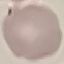 Malaria status: uninfected. Thin blood film. Cell patch, automatically extracted from a larger field of view and resized to 64 × 64 pixels. Photographed with a smartphone camera at the microscope eyepiece. Giemsa stain.